Report the malaria status of this cell.
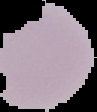

It is uninfected.

Summary:
  - Preparation: thin blood smear
  - Image size: 97×112 pixels
  - Image type: cell region segmented out of the field of view; surrounding area masked to black